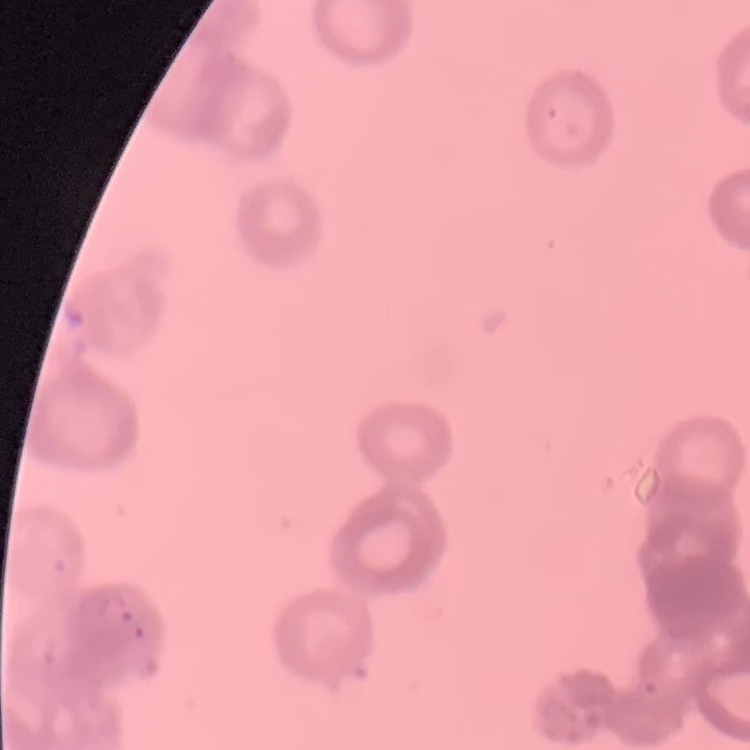

Summary:
  - Erythrocyte morphology: rouleaux formation
  - Preparation: thin blood smear
  - Stain: Field's or Giemsa
  - Image type: square crop of a larger photomicrograph